Assess the morphology of the red blood cells.
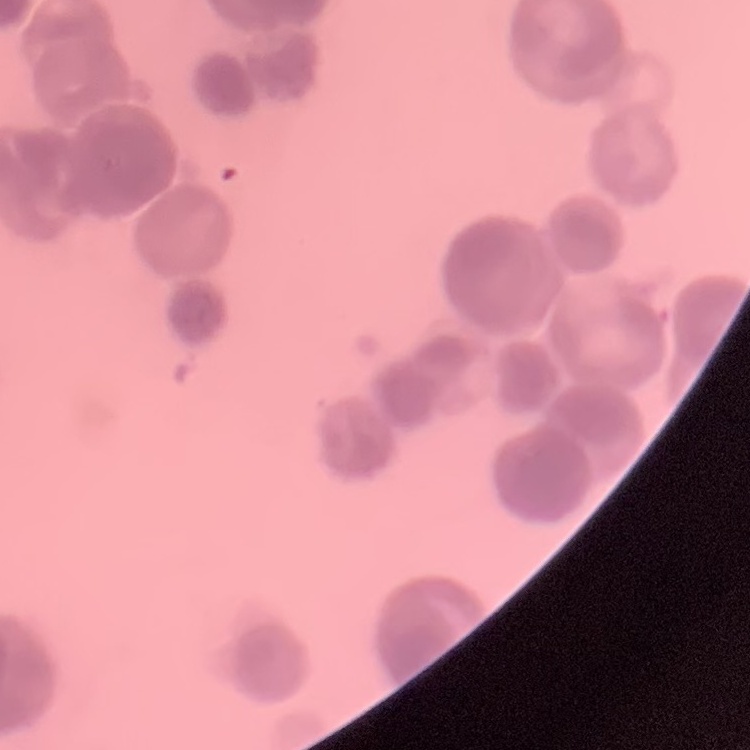

They show rouleaux formation.

stain = Field's or Giemsa
preparation = thin blood film
image type = one tile cut from a larger photomicrograph